Outline each blood parasite and name the species.
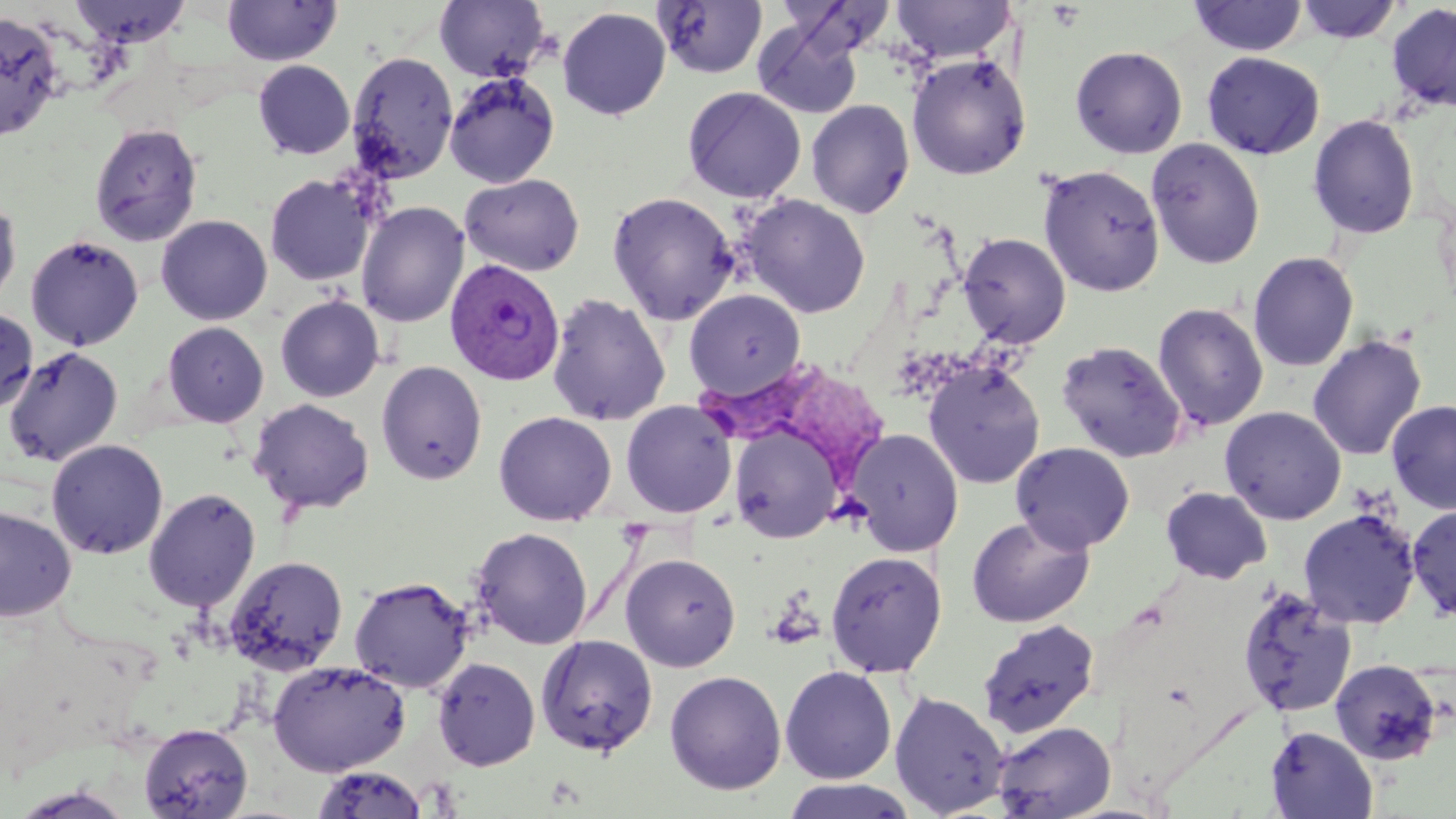
Approximate bounding boxes as named x1/y1/x2/y2 corners in pixels.
Plasmodium vivax-infected red blood cells: (x1=446, y1=258, x2=564, y2=385).
No Plasmodium falciparum, Plasmodium ovale, Plasmodium malariae, Babesia divergens, or Trypanosoma brucei observed.

slide-level diagnosis = Plasmodium vivax
image size = 1456×819 pixels
magnification = 1000x
stain = May-Grünwald-Giemsa
modality = light microscopy
field of view = single
uninfected red blood cell locations = approximate bounding boxes as named x1/y1/x2/y2 corners in pixels: (x1=67, y1=0, x2=193, y2=47), (x1=435, y1=0, x2=549, y2=82), (x1=890, y1=0, x2=1015, y2=63), (x1=1187, y1=0, x2=1308, y2=57), (x1=1294, y1=0, x2=1403, y2=45), (x1=222, y1=1, x2=343, y2=65), (x1=654, y1=1, x2=769, y2=78), (x1=1386, y1=2, x2=1456, y2=114), (x1=557, y1=7, x2=671, y2=121), (x1=0, y1=11, x2=66, y2=143), (x1=752, y1=19, x2=864, y2=120), (x1=1070, y1=45, x2=1188, y2=159), (x1=346, y1=49, x2=459, y2=183), (x1=1200, y1=51, x2=1325, y2=160), (x1=906, y1=53, x2=1031, y2=180), (x1=253, y1=60, x2=355, y2=160), (x1=444, y1=70, x2=560, y2=189), (x1=682, y1=86, x2=806, y2=204), (x1=805, y1=99, x2=915, y2=218), (x1=1307, y1=114, x2=1420, y2=239), (x1=89, y1=122, x2=203, y2=246), (x1=1146, y1=138, x2=1266, y2=270), (x1=1037, y1=164, x2=1166, y2=296), (x1=264, y1=173, x2=376, y2=286), (x1=459, y1=173, x2=585, y2=277), (x1=607, y1=191, x2=739, y2=325), (x1=741, y1=194, x2=872, y2=318), (x1=0, y1=195, x2=22, y2=311), (x1=356, y1=201, x2=469, y2=327), (x1=156, y1=215, x2=273, y2=325), (x1=957, y1=231, x2=1071, y2=348), (x1=26, y1=234, x2=143, y2=351), (x1=1248, y1=251, x2=1359, y2=372), (x1=684, y1=289, x2=806, y2=399), (x1=545, y1=292, x2=671, y2=426), (x1=275, y1=295, x2=385, y2=402), (x1=1152, y1=302, x2=1269, y2=432), (x1=0, y1=306, x2=38, y2=415), (x1=161, y1=321, x2=269, y2=428), (x1=1307, y1=333, x2=1428, y2=461), (x1=1056, y1=340, x2=1187, y2=463), (x1=3, y1=345, x2=123, y2=466), (x1=376, y1=360, x2=488, y2=485), (x1=923, y1=360, x2=1046, y2=489), (x1=248, y1=398, x2=374, y2=515), (x1=1386, y1=398, x2=1456, y2=515), (x1=620, y1=399, x2=738, y2=518), (x1=1220, y1=406, x2=1346, y2=524), (x1=493, y1=410, x2=617, y2=525), (x1=728, y1=423, x2=843, y2=544), (x1=847, y1=428, x2=965, y2=556), (x1=46, y1=438, x2=168, y2=559), (x1=1011, y1=441, x2=1135, y2=553), (x1=1159, y1=485, x2=1273, y2=584), (x1=143, y1=486, x2=262, y2=613), (x1=1406, y1=503, x2=1456, y2=622), (x1=0, y1=505, x2=77, y2=622), (x1=1298, y1=508, x2=1422, y2=629), (x1=966, y1=515, x2=1096, y2=628), (x1=470, y1=526, x2=593, y2=650), (x1=825, y1=550, x2=948, y2=678), (x1=619, y1=552, x2=742, y2=672), (x1=224, y1=555, x2=349, y2=675), (x1=349, y1=575, x2=474, y2=693), (x1=1235, y1=585, x2=1358, y2=718), (x1=976, y1=619, x2=1101, y2=738), (x1=535, y1=633, x2=658, y2=757), (x1=432, y1=656, x2=540, y2=770), (x1=1329, y1=658, x2=1444, y2=766), (x1=268, y1=659, x2=410, y2=776), (x1=780, y1=665, x2=898, y2=784), (x1=664, y1=670, x2=787, y2=795), (x1=889, y1=689, x2=1010, y2=818), (x1=991, y1=720, x2=1117, y2=819), (x1=138, y1=722, x2=253, y2=819), (x1=1265, y1=726, x2=1378, y2=818), (x1=312, y1=765, x2=431, y2=818), (x1=780, y1=779, x2=917, y2=818)
preparation = thin blood smear